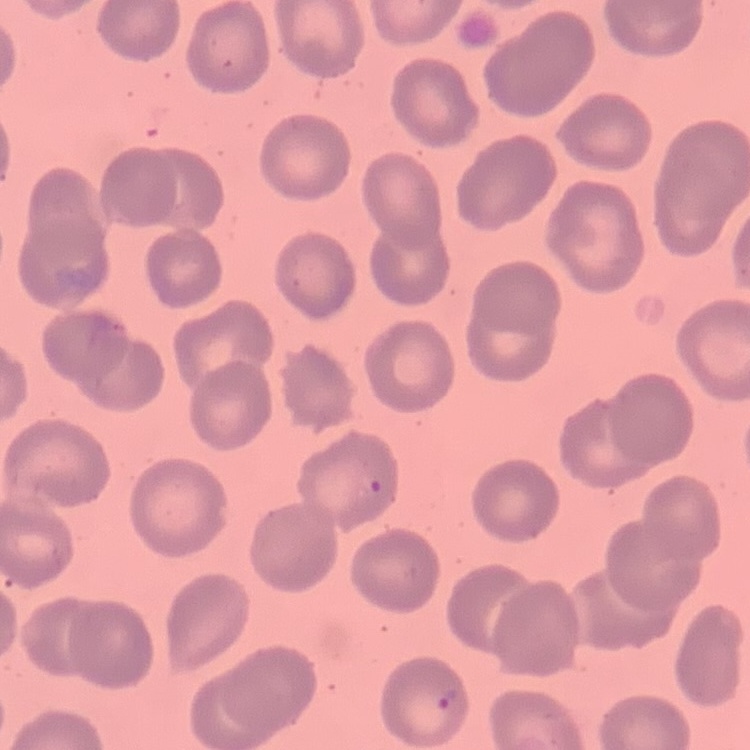
Summary:
  - Red blood cell morphology: no rouleaux formation
  - Image type: one tile cut from a larger photomicrograph
  - Preparation: thin blood smear
  - Stain: Field's or Giemsa